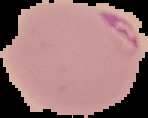
image type = cell region segmented out of the field of view; surrounding area masked to black
image size = 148×118 pixels
preparation = thin blood film
result = malaria parasites identified